Assess this cell for malaria.
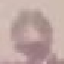
Uninfected.

Thin blood film. Cell patch, automatically extracted from a larger field of view and resized to 64 × 64 pixels. Photographed with a smartphone camera at the microscope eyepiece. Giemsa stain.